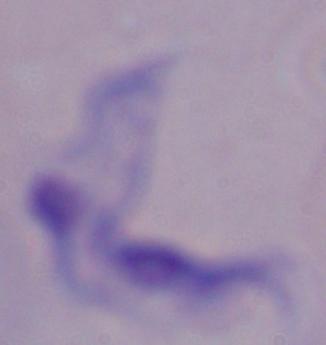

A trypanosome is shown. Captured at 1000x magnification. Photomicrograph.